Locate and identify every blood parasite.
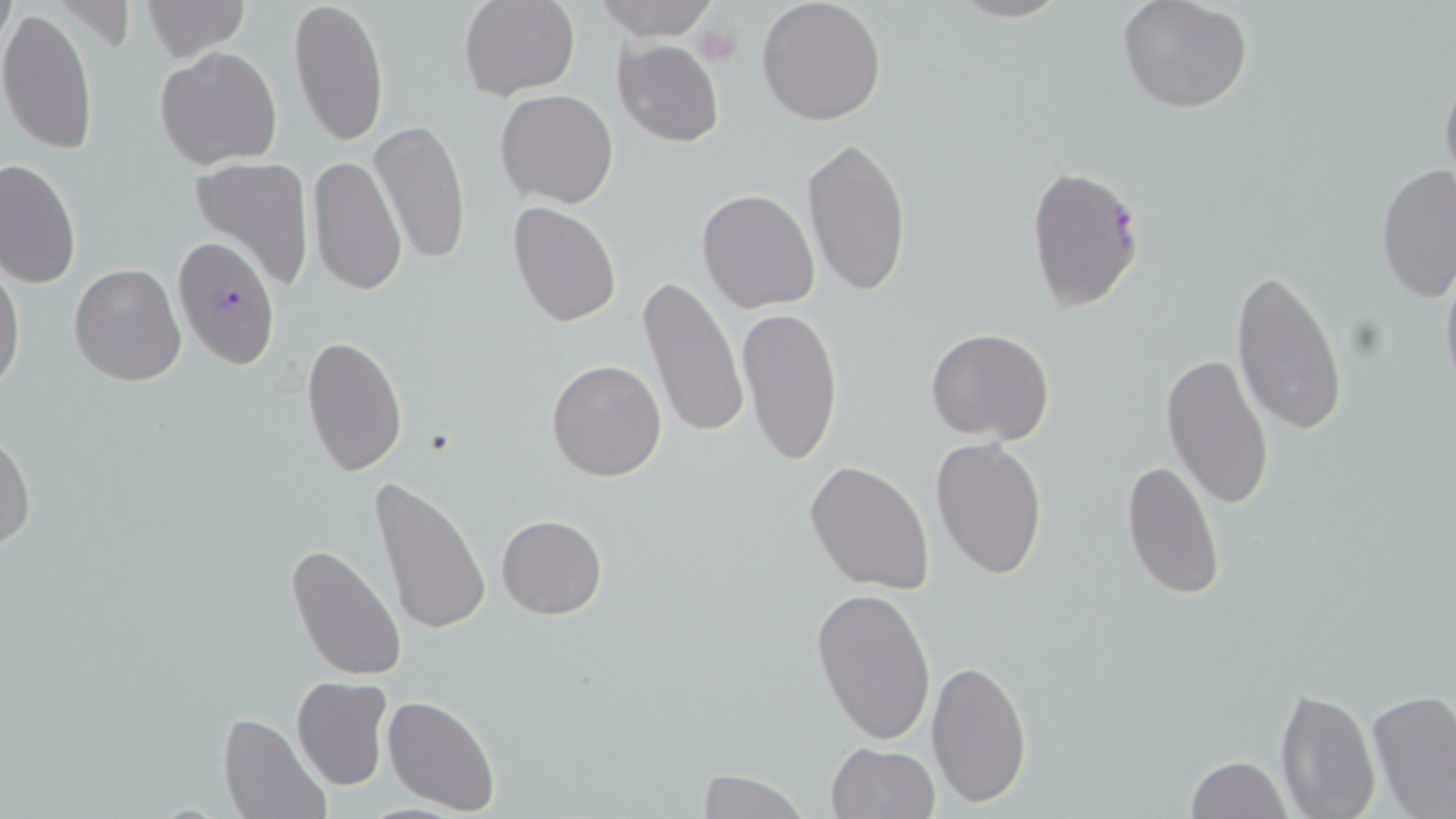

Approximate bounding boxes as [x1, y1, x2, y2] in pixels.
Plasmodium falciparum-infected red blood cells: [1025, 163, 1145, 312], [173, 238, 280, 367].
No Plasmodium ovale, Plasmodium malariae, Plasmodium vivax, Babesia divergens, or Trypanosoma brucei observed.

slide_level_diagnosis: Plasmodium falciparum
uninfected_red_blood_cell_locations: 'approximate bounding boxes as [x1, y1, x2, y2] in pixels: [289, 0, 389, 149], [460, 0, 580, 100], [593, 0, 720, 42], [757, 0, 888, 126], [945, 0, 1073, 23], [1116, 0, 1254, 115], [140, 1, 247, 61], [0, 7, 98, 156], [614, 40, 724, 148], [155, 46, 282, 170], [1439, 66, 1456, 193], [495, 89, 617, 208], [369, 119, 470, 266], [802, 137, 913, 300], [307, 154, 406, 299], [189, 155, 316, 293], [0, 157, 81, 290], [1375, 163, 1454, 304], [697, 189, 820, 312], [507, 201, 621, 326], [1439, 253, 1456, 406], [0, 258, 25, 400], [69, 263, 187, 386], [1231, 268, 1348, 435], [637, 277, 750, 442], [736, 308, 844, 467], [926, 328, 1055, 444], [301, 333, 408, 476], [1161, 354, 1275, 510], [546, 358, 668, 482], [0, 432, 35, 553], [931, 436, 1048, 579], [1121, 458, 1226, 601], [804, 460, 934, 595], [368, 476, 492, 638], [497, 514, 607, 620], [287, 543, 408, 683], [812, 586, 937, 745], [925, 658, 1032, 809], [291, 676, 391, 791], [1275, 687, 1379, 819], [1366, 688, 1456, 818], [383, 694, 500, 814], [221, 712, 332, 819], [825, 742, 941, 819], [1185, 756, 1290, 818], [692, 767, 811, 819]'
image_size: 1456×819 pixels
magnification: 1000x
modality: optical microscopy
platelet_locations: 'approximate bounding boxes as [x1, y1, x2, y2] in pixels: [694, 24, 742, 67]'
preparation: thin blood film
field_of_view: single
stain: May-Grünwald-Giemsa